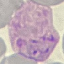

Summary:
  - Result: malaria parasites identified
  - Stain: Giemsa
  - Image type: automatically extracted cell patch, resized to 64 × 64 pixels
  - Capture: smartphone camera at the microscope eyepiece
  - Preparation: thin smear